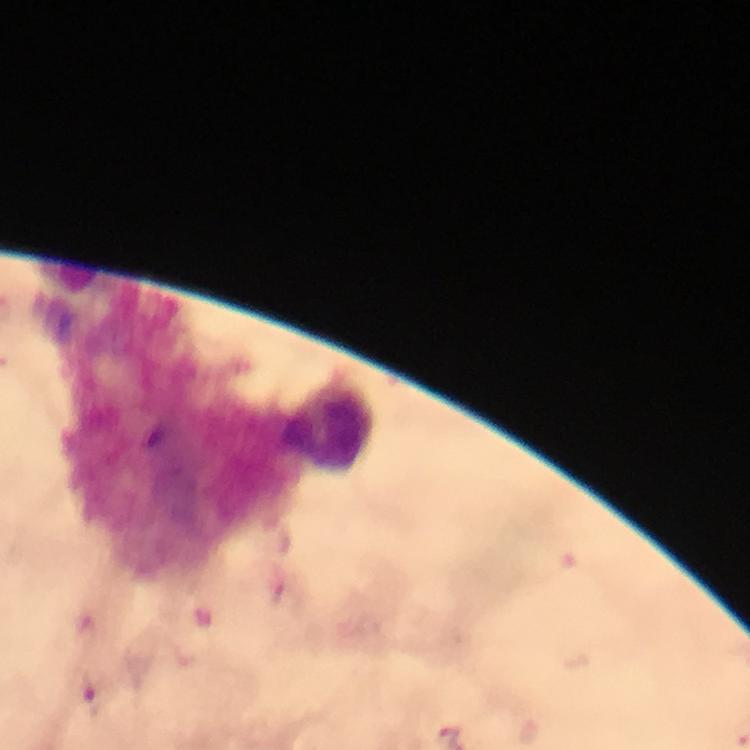
Approximate centers as (x, y) in pixels. Malaria parasite locations: (445, 735). Leukocyte locations: (327, 425). Thick smear. 100x magnification. Smartphone photograph taken through a microscope. Image is 750×750 pixels. From a diagnostic examination for malaria. A crop from one field of view. Immersion oil applied. Giemsa stain.